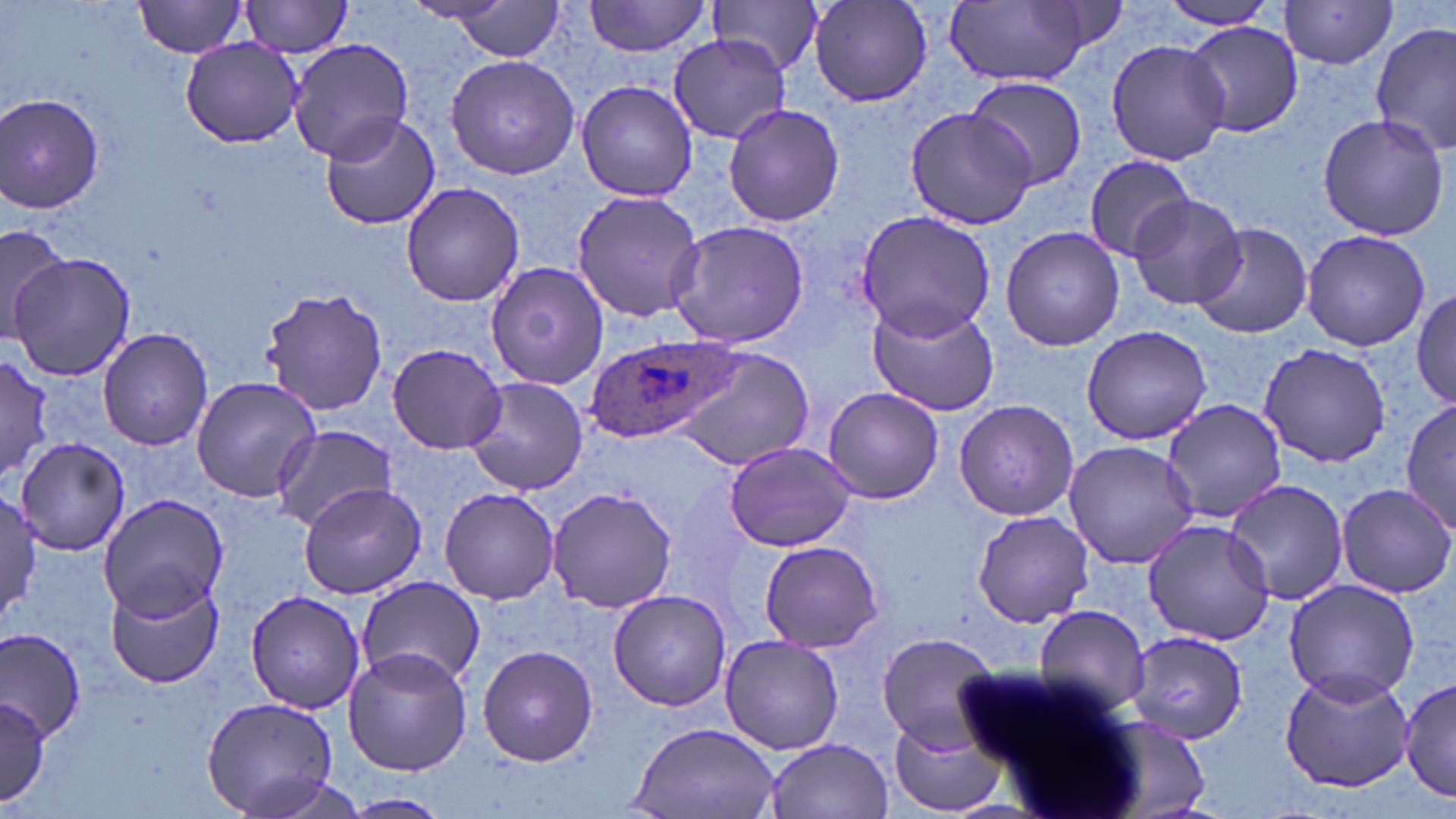
slide_level_diagnosis: Plasmodium ovale
magnification: 1000x
uninfected_red_blood_cell_locations: 'approximate bounding boxes as named x1/y1/x2/y2 corners in pixels: (x1=134, y1=0, x2=251, y2=59), (x1=240, y1=0, x2=355, y2=58), (x1=440, y1=0, x2=570, y2=65), (x1=584, y1=0, x2=710, y2=58), (x1=709, y1=0, x2=825, y2=76), (x1=809, y1=0, x2=933, y2=109), (x1=942, y1=0, x2=1102, y2=87), (x1=1156, y1=1, x2=1282, y2=31), (x1=1279, y1=1, x2=1399, y2=69), (x1=1183, y1=21, x2=1304, y2=137), (x1=1371, y1=24, x2=1456, y2=156), (x1=178, y1=35, x2=307, y2=149), (x1=667, y1=35, x2=791, y2=143), (x1=288, y1=36, x2=413, y2=164), (x1=1104, y1=39, x2=1232, y2=167), (x1=445, y1=56, x2=581, y2=178), (x1=965, y1=75, x2=1087, y2=191), (x1=575, y1=80, x2=698, y2=202), (x1=1, y1=93, x2=105, y2=214), (x1=721, y1=101, x2=848, y2=227), (x1=904, y1=105, x2=1037, y2=231), (x1=318, y1=112, x2=440, y2=231), (x1=1315, y1=113, x2=1451, y2=242), (x1=1083, y1=155, x2=1196, y2=262), (x1=400, y1=180, x2=524, y2=308), (x1=570, y1=190, x2=705, y2=323), (x1=1125, y1=194, x2=1246, y2=311), (x1=853, y1=209, x2=997, y2=342), (x1=666, y1=220, x2=810, y2=350), (x1=0, y1=221, x2=72, y2=346), (x1=1190, y1=221, x2=1312, y2=340), (x1=999, y1=225, x2=1127, y2=353), (x1=1300, y1=229, x2=1430, y2=352), (x1=6, y1=250, x2=134, y2=382), (x1=486, y1=261, x2=609, y2=391), (x1=262, y1=286, x2=389, y2=418), (x1=1413, y1=286, x2=1455, y2=411), (x1=867, y1=301, x2=998, y2=418), (x1=1081, y1=324, x2=1213, y2=446), (x1=97, y1=327, x2=214, y2=451), (x1=387, y1=343, x2=507, y2=454), (x1=1257, y1=343, x2=1393, y2=466), (x1=674, y1=348, x2=815, y2=472), (x1=0, y1=357, x2=54, y2=485), (x1=190, y1=376, x2=321, y2=503), (x1=464, y1=376, x2=590, y2=497), (x1=822, y1=389, x2=944, y2=503), (x1=1400, y1=395, x2=1454, y2=537), (x1=953, y1=397, x2=1078, y2=521), (x1=1161, y1=397, x2=1286, y2=525), (x1=270, y1=424, x2=396, y2=531), (x1=14, y1=437, x2=131, y2=553), (x1=723, y1=440, x2=856, y2=552), (x1=1063, y1=441, x2=1200, y2=570), (x1=1224, y1=478, x2=1352, y2=606), (x1=298, y1=482, x2=426, y2=599), (x1=1335, y1=482, x2=1456, y2=600), (x1=438, y1=486, x2=560, y2=604), (x1=547, y1=486, x2=679, y2=613), (x1=1, y1=493, x2=42, y2=627), (x1=98, y1=494, x2=227, y2=620), (x1=970, y1=508, x2=1097, y2=626), (x1=1141, y1=520, x2=1277, y2=645), (x1=757, y1=539, x2=885, y2=653), (x1=106, y1=576, x2=225, y2=691), (x1=352, y1=577, x2=487, y2=694), (x1=1284, y1=579, x2=1422, y2=702), (x1=243, y1=590, x2=366, y2=715), (x1=608, y1=590, x2=732, y2=710), (x1=1030, y1=605, x2=1152, y2=716), (x1=0, y1=626, x2=86, y2=739), (x1=1122, y1=630, x2=1251, y2=744), (x1=875, y1=631, x2=1004, y2=748), (x1=720, y1=634, x2=845, y2=755), (x1=477, y1=643, x2=599, y2=767), (x1=343, y1=647, x2=474, y2=775), (x1=1279, y1=668, x2=1413, y2=792), (x1=1401, y1=678, x2=1456, y2=801), (x1=199, y1=696, x2=341, y2=819), (x1=0, y1=698, x2=53, y2=804), (x1=1093, y1=716, x2=1213, y2=819), (x1=887, y1=717, x2=1010, y2=818), (x1=626, y1=721, x2=783, y2=819), (x1=765, y1=737, x2=893, y2=819), (x1=231, y1=770, x2=369, y2=819), (x1=338, y1=793, x2=452, y2=818)'
plasmodium_ovale_infected_red_blood_cell_locations: 'approximate bounding boxes as named x1/y1/x2/y2 corners in pixels: (x1=585, y1=336, x2=743, y2=447)'
stain: May-Grünwald-Giemsa
field_of_view: one of a larger specimen
preparation: thin blood film
modality: light microscopy
image_size: 1456×819 pixels